Locate every blood parasite and identify its species.
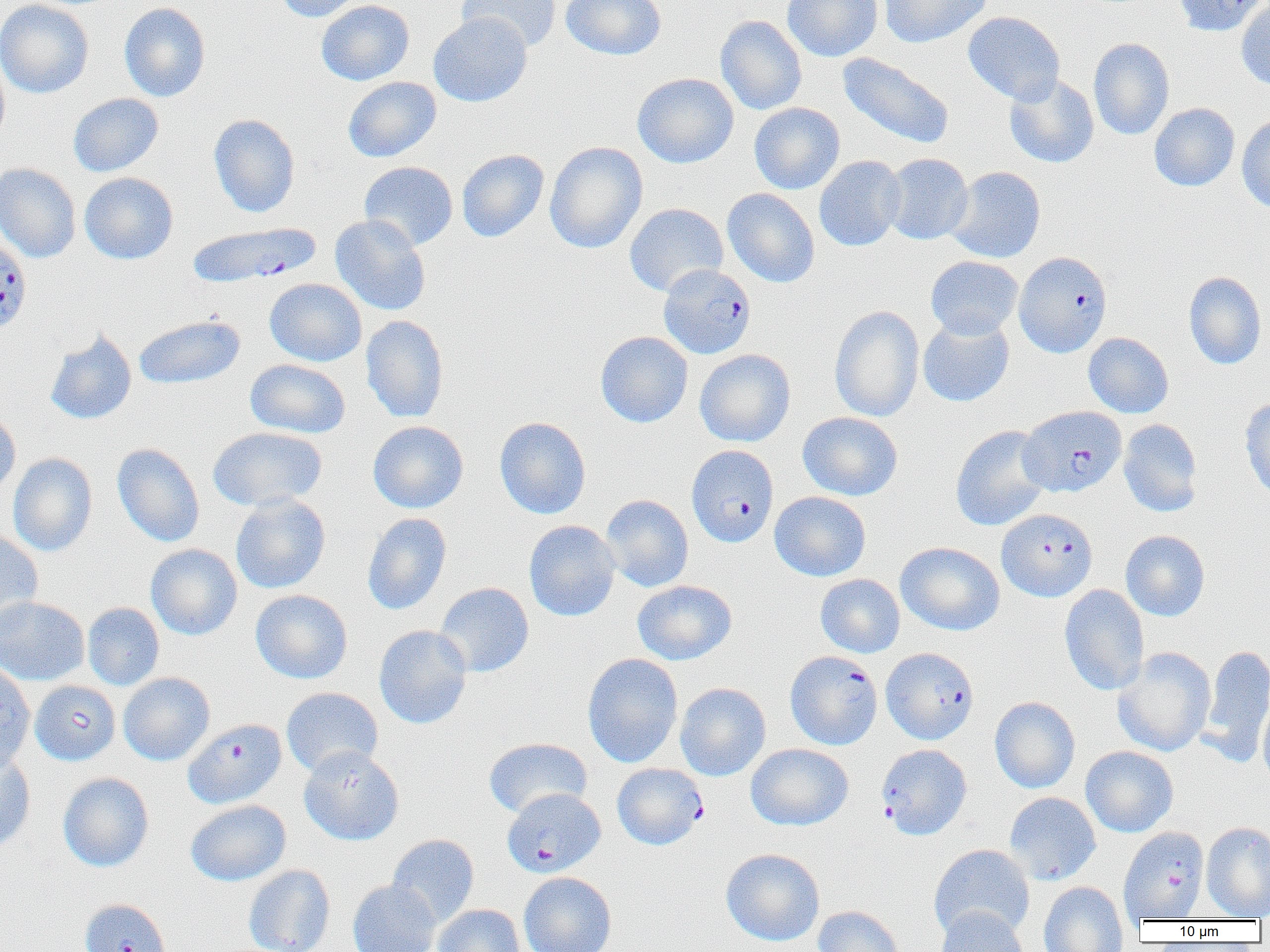

Approximate bounding boxes as named x1/y1/x2/y2 corners in pixels.
Plasmodium falciparum-infected red blood cells: (x1=187, y1=223, x2=322, y2=288), (x1=0, y1=243, x2=44, y2=330), (x1=1014, y1=251, x2=1111, y2=357), (x1=659, y1=264, x2=755, y2=359), (x1=1019, y1=406, x2=1127, y2=497), (x1=687, y1=445, x2=778, y2=547), (x1=996, y1=508, x2=1097, y2=601), (x1=881, y1=647, x2=977, y2=744), (x1=785, y1=650, x2=882, y2=750), (x1=184, y1=719, x2=286, y2=808), (x1=876, y1=743, x2=972, y2=840), (x1=612, y1=763, x2=708, y2=850), (x1=502, y1=787, x2=605, y2=877), (x1=1118, y1=827, x2=1209, y2=921), (x1=79, y1=897, x2=172, y2=952).
No Plasmodium ovale, Plasmodium malariae, Plasmodium vivax, Babesia divergens, or Trypanosoma brucei observed.

Uninfected red blood cell locations: (x1=0, y1=0, x2=94, y2=98), (x1=275, y1=0, x2=366, y2=22), (x1=316, y1=0, x2=414, y2=86), (x1=457, y1=0, x2=560, y2=53), (x1=561, y1=0, x2=666, y2=60), (x1=783, y1=0, x2=882, y2=62), (x1=879, y1=0, x2=991, y2=48), (x1=1175, y1=0, x2=1266, y2=35), (x1=1236, y1=0, x2=1270, y2=90), (x1=119, y1=2, x2=210, y2=102), (x1=963, y1=11, x2=1065, y2=104), (x1=428, y1=13, x2=532, y2=107), (x1=715, y1=15, x2=807, y2=115), (x1=1088, y1=38, x2=1174, y2=140), (x1=837, y1=52, x2=955, y2=150), (x1=0, y1=55, x2=10, y2=148), (x1=632, y1=73, x2=739, y2=168), (x1=1004, y1=74, x2=1099, y2=168), (x1=343, y1=76, x2=441, y2=162), (x1=68, y1=93, x2=164, y2=177), (x1=749, y1=102, x2=845, y2=194), (x1=1149, y1=103, x2=1239, y2=191), (x1=1236, y1=112, x2=1270, y2=214), (x1=209, y1=113, x2=300, y2=217), (x1=544, y1=141, x2=648, y2=253), (x1=457, y1=149, x2=549, y2=242), (x1=882, y1=153, x2=973, y2=244), (x1=814, y1=156, x2=906, y2=252), (x1=359, y1=161, x2=458, y2=250), (x1=0, y1=162, x2=81, y2=262), (x1=946, y1=166, x2=1045, y2=263), (x1=79, y1=172, x2=178, y2=264), (x1=722, y1=188, x2=820, y2=287), (x1=624, y1=202, x2=729, y2=297), (x1=330, y1=214, x2=431, y2=316), (x1=925, y1=256, x2=1023, y2=340), (x1=1184, y1=271, x2=1267, y2=370), (x1=264, y1=278, x2=366, y2=366), (x1=829, y1=305, x2=925, y2=422), (x1=133, y1=315, x2=245, y2=389), (x1=361, y1=315, x2=448, y2=423), (x1=918, y1=317, x2=1014, y2=407), (x1=45, y1=330, x2=137, y2=424), (x1=595, y1=331, x2=693, y2=427), (x1=1084, y1=332, x2=1173, y2=418), (x1=695, y1=349, x2=795, y2=446), (x1=246, y1=359, x2=351, y2=438), (x1=1239, y1=394, x2=1270, y2=504), (x1=0, y1=410, x2=21, y2=498), (x1=798, y1=411, x2=903, y2=500), (x1=494, y1=416, x2=591, y2=519), (x1=1118, y1=419, x2=1204, y2=517), (x1=368, y1=421, x2=468, y2=513), (x1=950, y1=425, x2=1052, y2=531), (x1=208, y1=426, x2=327, y2=512), (x1=112, y1=443, x2=205, y2=547), (x1=8, y1=452, x2=98, y2=556), (x1=769, y1=491, x2=871, y2=581), (x1=231, y1=494, x2=330, y2=594), (x1=600, y1=494, x2=694, y2=592), (x1=362, y1=512, x2=452, y2=615), (x1=523, y1=520, x2=620, y2=621), (x1=0, y1=528, x2=43, y2=627), (x1=1120, y1=529, x2=1210, y2=621), (x1=896, y1=542, x2=1005, y2=635), (x1=145, y1=543, x2=243, y2=640), (x1=815, y1=574, x2=905, y2=658), (x1=632, y1=580, x2=737, y2=665), (x1=435, y1=582, x2=534, y2=677), (x1=1059, y1=584, x2=1150, y2=695), (x1=250, y1=589, x2=352, y2=684), (x1=0, y1=596, x2=89, y2=685), (x1=83, y1=602, x2=165, y2=690), (x1=374, y1=625, x2=472, y2=729), (x1=1201, y1=643, x2=1270, y2=766), (x1=1113, y1=647, x2=1216, y2=757), (x1=582, y1=653, x2=683, y2=768), (x1=0, y1=662, x2=35, y2=772), (x1=118, y1=672, x2=215, y2=766), (x1=30, y1=680, x2=120, y2=765), (x1=675, y1=682, x2=771, y2=780), (x1=281, y1=687, x2=383, y2=777), (x1=1257, y1=690, x2=1270, y2=788), (x1=989, y1=696, x2=1080, y2=793), (x1=484, y1=737, x2=592, y2=818), (x1=745, y1=743, x2=854, y2=830), (x1=299, y1=746, x2=404, y2=845), (x1=1080, y1=746, x2=1178, y2=837), (x1=0, y1=751, x2=35, y2=854), (x1=58, y1=772, x2=154, y2=872), (x1=1004, y1=792, x2=1101, y2=885), (x1=185, y1=800, x2=291, y2=885), (x1=1201, y1=821, x2=1270, y2=919), (x1=387, y1=833, x2=479, y2=927), (x1=929, y1=844, x2=1035, y2=942), (x1=721, y1=848, x2=825, y2=946), (x1=243, y1=864, x2=335, y2=952), (x1=518, y1=872, x2=616, y2=952), (x1=347, y1=879, x2=441, y2=952), (x1=1038, y1=881, x2=1129, y2=952), (x1=432, y1=904, x2=525, y2=952), (x1=813, y1=906, x2=905, y2=952), (x1=935, y1=906, x2=1030, y2=952). Slide-level diagnosis: Plasmodium falciparum. Optical microscopy. Image is 1270×952 pixels. Captured at 1000x magnification. Thin blood smear. One field of a larger specimen.